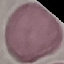
Result: no malaria parasites detected. Giemsa-stained preparation. Cell patch, automatically extracted from a larger field of view and resized to 64 × 64 pixels. Acquired by smartphone through the microscope eyepiece. Thin blood smear.